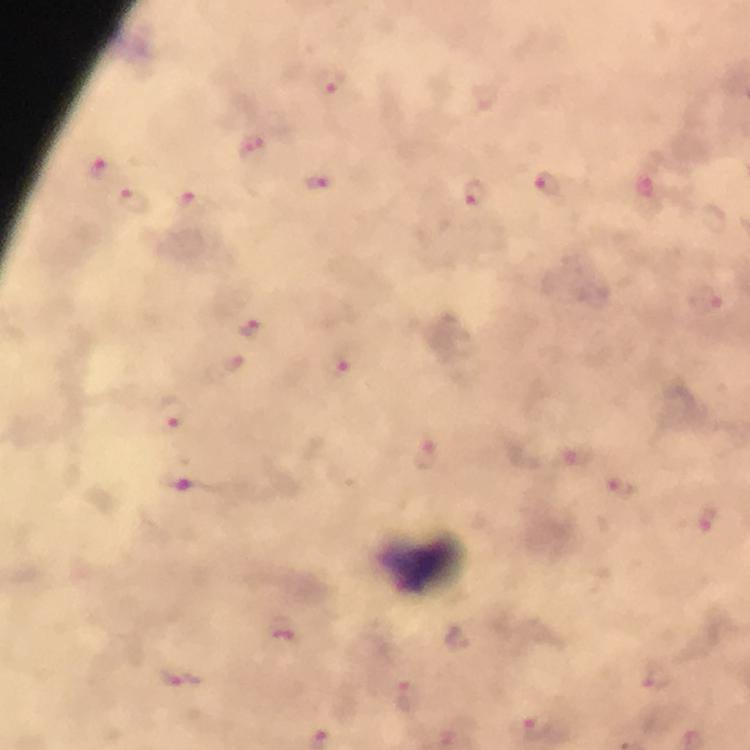
preparation = thick blood smear
capture = smartphone camera through the microscope
cropped from = one field of view
magnification = 100x
leukocyte locations = approximate centers as {x, y} in pixels: {423, 566}
context = from a diagnostic examination for malaria
stain = Giemsa
malaria parasite locations = approximate centers as {x, y} in pixels: {330, 83}, {254, 150}, {102, 167}, {318, 183}, {548, 187}, {474, 193}, {135, 198}, {193, 202}, {705, 300}, {252, 327}, {343, 364}, {174, 412}, {426, 454}, {578, 455}, {188, 478}, {622, 485}, {709, 518}, {283, 629}, {183, 676}, {657, 679}, {409, 695}, {540, 728}
immersion oil = used
image size = 750×750 pixels